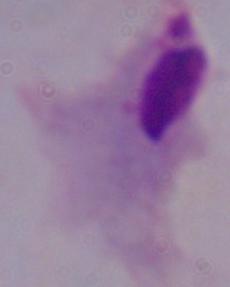

Summary:
  - Magnification: 1000x
  - Identification: trichomonad
  - Modality: photomicrograph